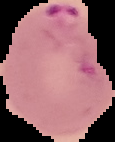
result = malaria parasites detected
image size = 115×142 pixels
image type = cell region segmented out of the field of view; surrounding area masked to black
preparation = thin blood film